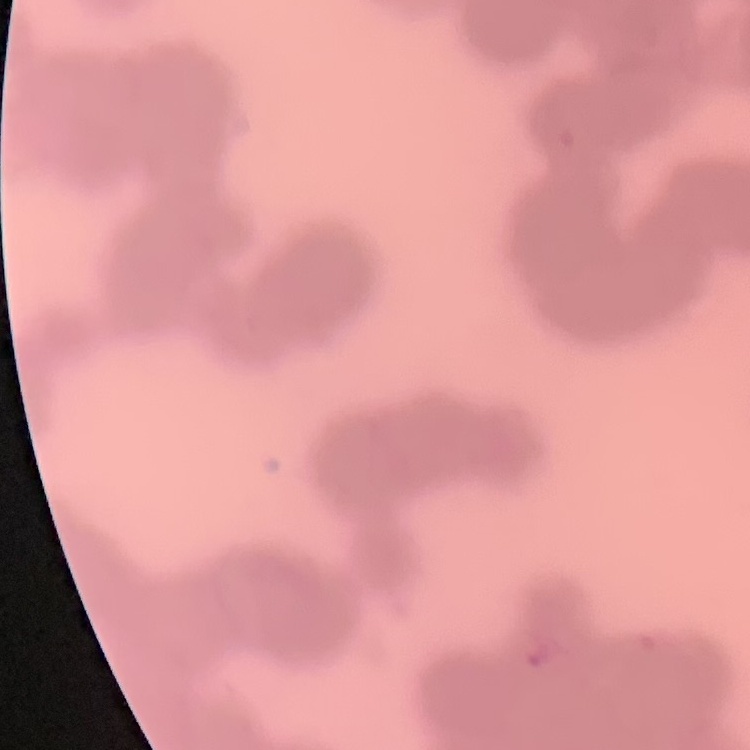

erythrocyte morphology = rouleaux formation
image type = one tile cut from a larger photomicrograph
stain = Field's or Giemsa
preparation = thin peripheral smear